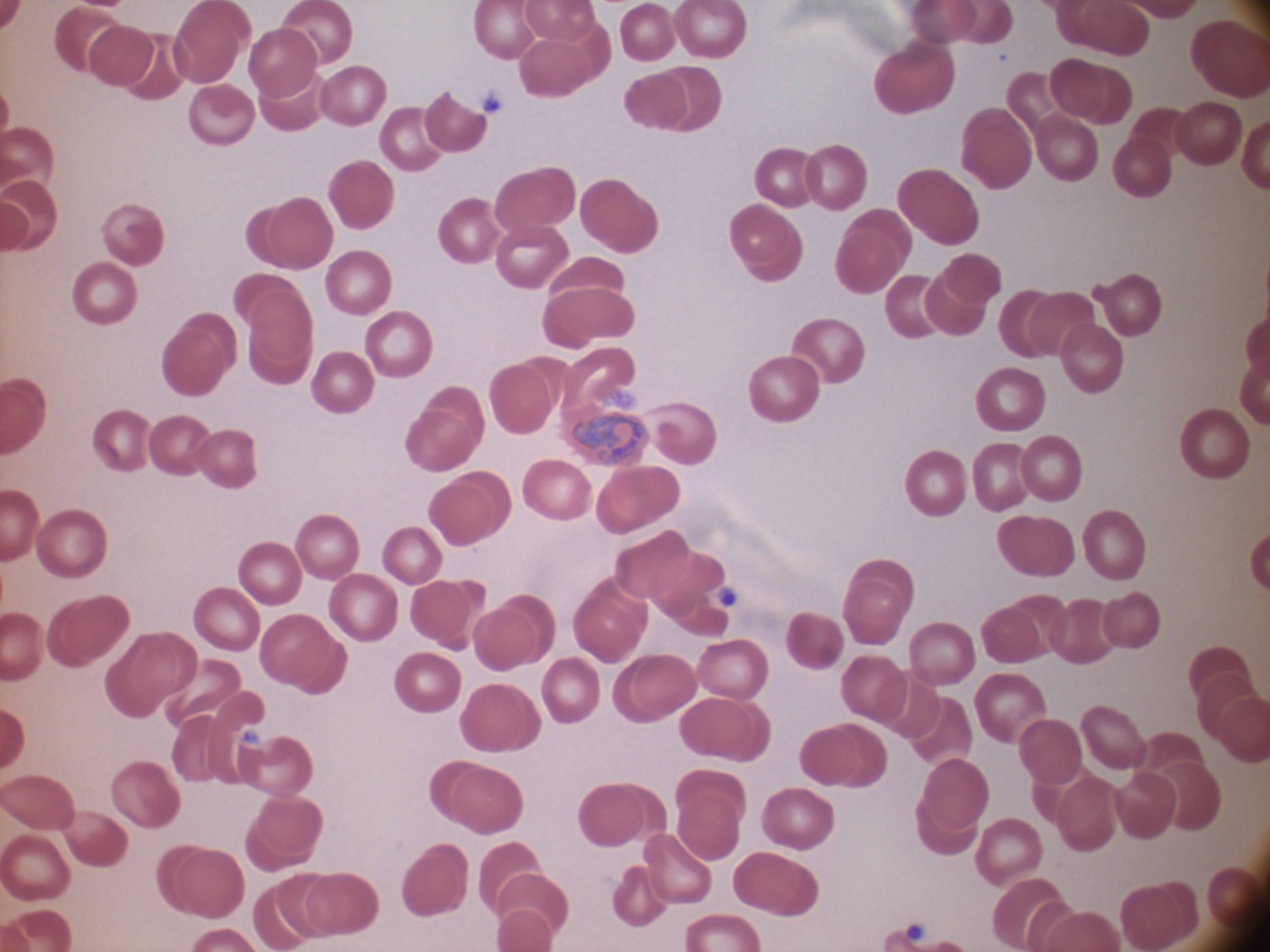 Approximate bounding boxes as named x1/y1/x2/y2 corners in pixels, from the source annotation, which is not necessarily exhaustive. Trophozoite locations: (x1=570, y1=412, x2=646, y2=462). Captured at 100x magnification. Leica DM2000 optical microscope with a built-in camera. Thin blood film. Giemsa stain. Image is 1270×952 pixels. One field from this slide. Species: Plasmodium ovale.